Identify the cell.
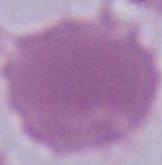
An erythrocyte.

Summary:
  - Modality: micrograph
  - Magnification: 1000x